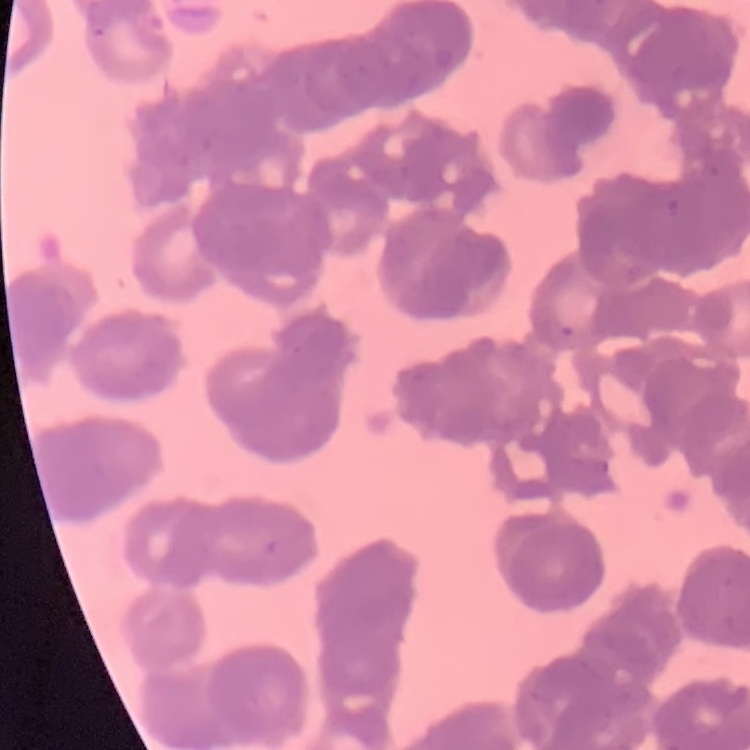 The red blood cells exhibit rouleaux formation. Thin blood film. Stained with either Field's or Giemsa. One tile cut from a larger photomicrograph.